Give the position of every Plasmodium parasite visible.
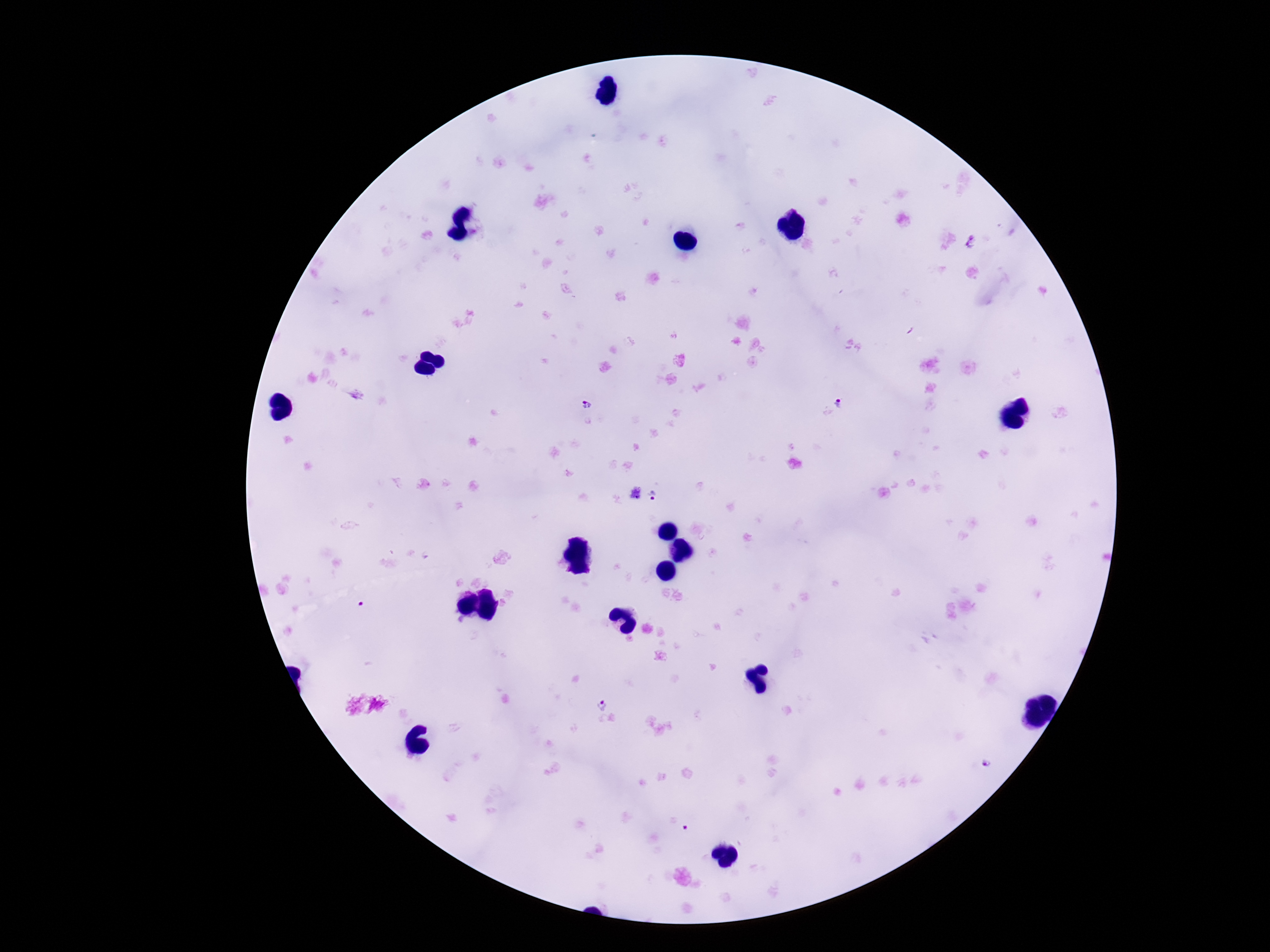
Approximate object centers, in pixels from the top-left corner.
Plasmodium parasites: (x=837, y=402), (x=585, y=404), (x=652, y=494), (x=601, y=703), (x=987, y=764).

magnification = 100x
patient malaria status = infected
field of view = single
preparation = thick blood film
capture = smartphone camera through the microscope eyepiece
stain = Giemsa
image size = 1270×952 pixels